Comment on the morphology of the red blood cells.
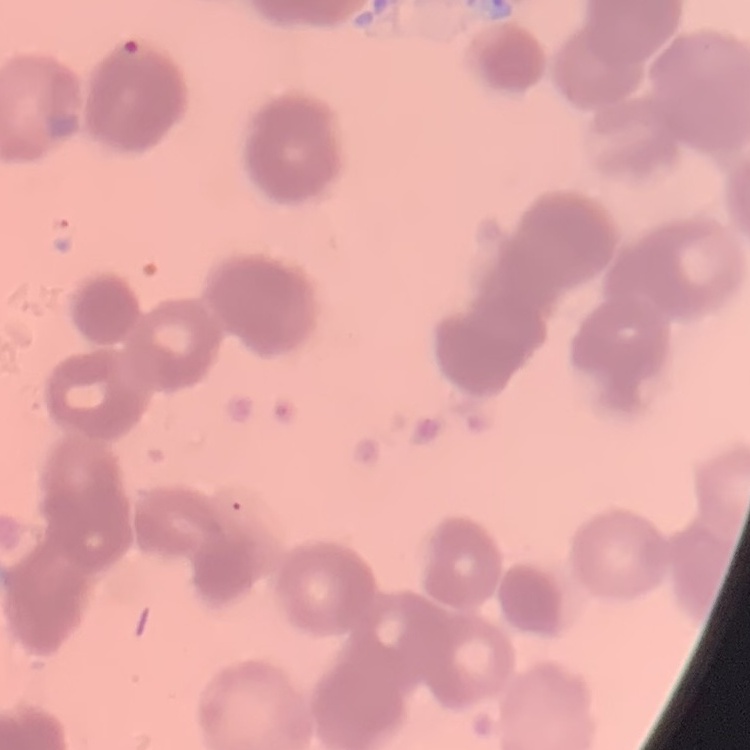

They show rouleaux formation.

image type = one tile cut from a larger photomicrograph
stain = Field's or Giemsa
preparation = thin blood smear